Assess this cell for malaria.
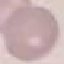

It is uninfected.

Automatically extracted cell patch, resized to 64 × 64 pixels. Giemsa stain. Thin smear of blood. Photographed with a smartphone camera at the microscope eyepiece.